Classify this cell by malaria status.
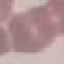

It is uninfected.

Summary:
  - Capture: smartphone through the microscope eyepiece
  - Image type: cell patch, automatically extracted from a larger field of view and resized to 64 × 64 pixels
  - Stain: Giemsa
  - Preparation: thin blood film